Give the position of every malaria parasite.
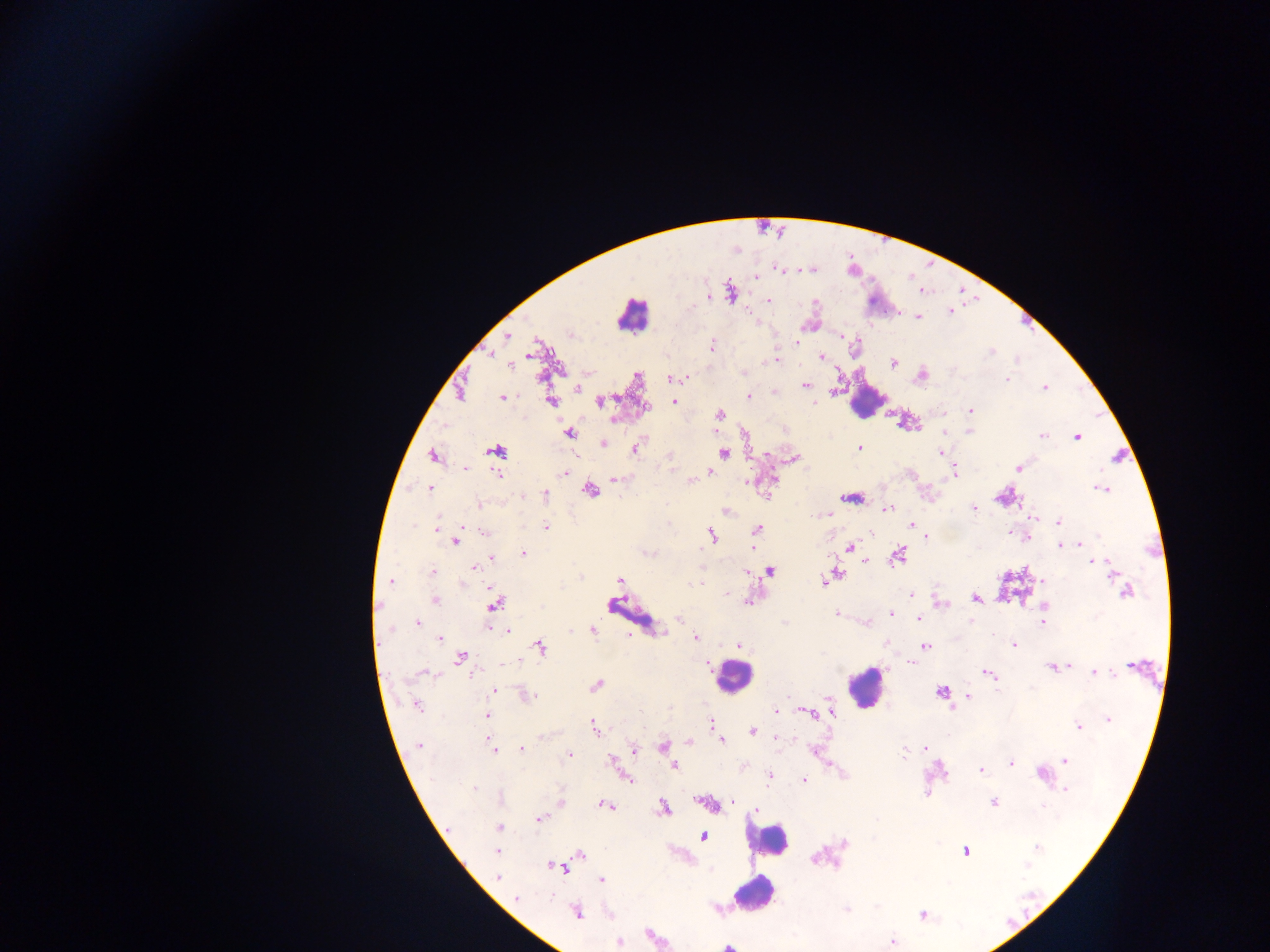
Approximate centers as {x, y} in pixels.
Malaria parasites: {781, 269}, {756, 276}, {730, 292}, {710, 295}, {767, 300}, {949, 310}, {917, 316}, {841, 336}, {507, 337}, {709, 347}, {489, 353}, {530, 353}, {821, 357}, {776, 360}, {892, 362}, {511, 364}, {922, 375}, {670, 377}, {679, 378}, {686, 379}, {1005, 379}, {806, 385}, {1044, 387}, {576, 388}, {461, 391}, {749, 396}, {502, 398}, {551, 401}, {599, 401}, {674, 401}, {969, 410}, {718, 415}, {614, 418}, {905, 421}, {969, 431}, {568, 433}, {1042, 435}, {1077, 437}, {603, 443}, {635, 447}, {859, 448}, {494, 450}, {941, 453}, {723, 454}, {433, 455}, {766, 455}, {671, 456}, {793, 458}, {464, 468}, {1019, 468}, {954, 470}, {709, 471}, {497, 473}, {566, 473}, {615, 479}, {772, 480}, {690, 481}, {747, 481}, {429, 488}, {1102, 488}, {590, 490}, {545, 494}, {767, 495}, {1003, 495}, {853, 498}, {479, 504}, {973, 508}, {887, 509}, {726, 511}, {825, 514}, {1032, 519}, {1058, 522}, {910, 524}, {546, 527}, {438, 528}, {757, 530}, {484, 532}, {1013, 533}, {711, 535}, {925, 535}, {1025, 535}, {456, 540}, {1059, 545}, {849, 547}, {523, 552}, {896, 555}, {490, 558}, {866, 560}, {1092, 561}, {474, 567}, {769, 571}, {432, 572}, {1112, 573}, {836, 574}, {620, 579}, {823, 580}, {389, 582}, {700, 582}, {1044, 582}, {1121, 583}, {1125, 591}, {728, 592}, {911, 595}, {975, 598}, {433, 599}, {748, 601}, {939, 603}, {494, 604}, {1045, 606}, {891, 613}, {836, 614}, {680, 617}, {918, 618}, {1042, 622}, {417, 623}, {867, 623}, {490, 626}, {506, 629}, {590, 630}, {440, 638}, {695, 638}, {1013, 644}, {738, 645}, {925, 645}, {539, 647}, {461, 657}, {909, 662}, {706, 664}, {1133, 665}, {1067, 666}, {1052, 667}, {422, 672}, {1094, 672}, {988, 673}, {596, 684}, {493, 691}, {940, 692}, {524, 693}, {967, 694}, {416, 704}, {775, 710}, {805, 712}, {830, 712}, {812, 714}, {488, 715}, {1108, 718}, {710, 722}, {1078, 726}, {593, 727}, {752, 731}, {720, 740}, {688, 741}, {418, 745}, {492, 747}, {663, 747}, {634, 748}, {521, 749}, {924, 749}, {815, 751}, {904, 751}, {568, 755}, {1064, 760}, {613, 762}, {1010, 763}, {829, 764}, {674, 766}, {743, 766}, {980, 770}, {1042, 773}, {769, 776}, {627, 778}, {804, 780}, {474, 788}, {1066, 788}, {733, 801}, {560, 802}, {992, 802}, {708, 804}, {603, 805}, {663, 808}, {757, 811}, {539, 818}, {499, 827}, {702, 836}, {1037, 846}, {497, 850}, {964, 850}, {580, 854}, {556, 866}, {497, 878}, {601, 879}, {515, 898}, {575, 912}, {922, 914}, {892, 940}, {619, 941}.

Summary:
  - Leukocyte locations: {632, 315}, {865, 399}, {733, 676}, {865, 687}, {768, 839}, {754, 894}, {728, 945}
  - Country: Ghana
  - Field of view: single
  - Capture: mobile-phone photograph through a microscope
  - Image size: 1270×952 pixels
  - Preparation: thick blood smear